Classify this cell by malaria status.
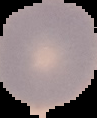

It is uninfected.

Image is 97×118 pixels. From a thin blood smear. The area outside the segmented cell region is set to black.